Classify this cell by malaria status.
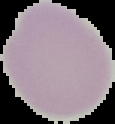

It is uninfected.

Summary:
  - Image size: 115×124 pixels
  - Preparation: thin blood smear
  - Image type: segmented cell region with the area outside set to black